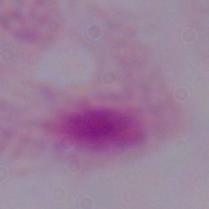

Summary:
  - Magnification: 1000x
  - Identification: trichomonad
  - Modality: micrograph